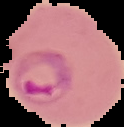

image_size: 124×127 pixels
preparation: thin blood film
image_type: segmented cell region on a black background
result: Plasmodium parasites identified